Name the cell type shown.
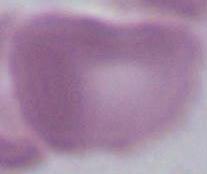
This is an erythrocyte.

Captured at 1000x magnification. Photomicrograph.